Identify the parasite.
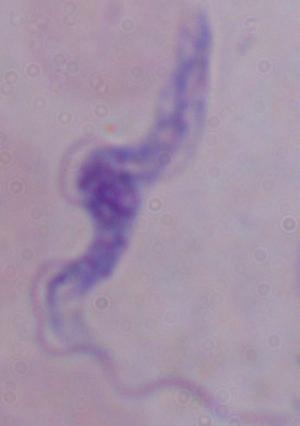

A trypanosome.

{
  "modality": "photomicrograph",
  "magnification": "1000x"
}